Report the malaria status of this cell.
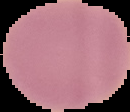
It is uninfected.

preparation = thin blood film
image size = 130×112 pixels
image type = segmented cell region with the area outside set to black